Report the malaria status of this cell.
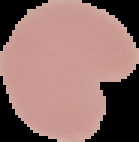

It is uninfected.

image size = 139×142 pixels
image type = segmented cell region on a black background
preparation = thin blood film